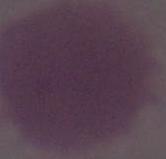

{
  "identification": "red blood cell",
  "modality": "micrograph",
  "magnification": "1000x"
}